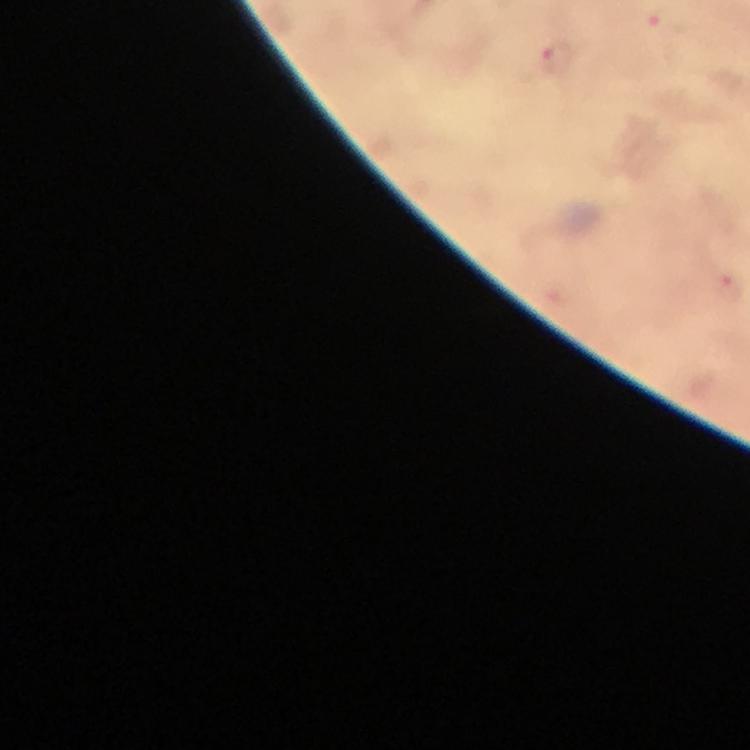

Approximate centers as (x, y) in pixels.
Summary:
  - Plasmodium parasite locations: (559, 62)
  - Context: from a diagnostic examination for malaria
  - Immersion oil: applied
  - Preparation: thick smear
  - Cropped from: one field of view
  - Magnification: 100x
  - Image size: 750×750 pixels
  - Capture: smartphone photograph through a microscope
  - Stain: Giemsa